Classify this cell by malaria status.
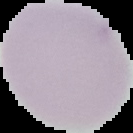
Uninfected.

image size = 133×133 pixels
image type = segmented cell region with the area outside set to black
preparation = thin blood smear